Classify this cell by malaria status.
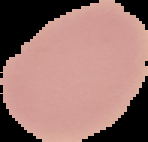
It is uninfected.

Image is 148×142 pixels. The area outside the segmented cell region is set to black. From a thin blood film.